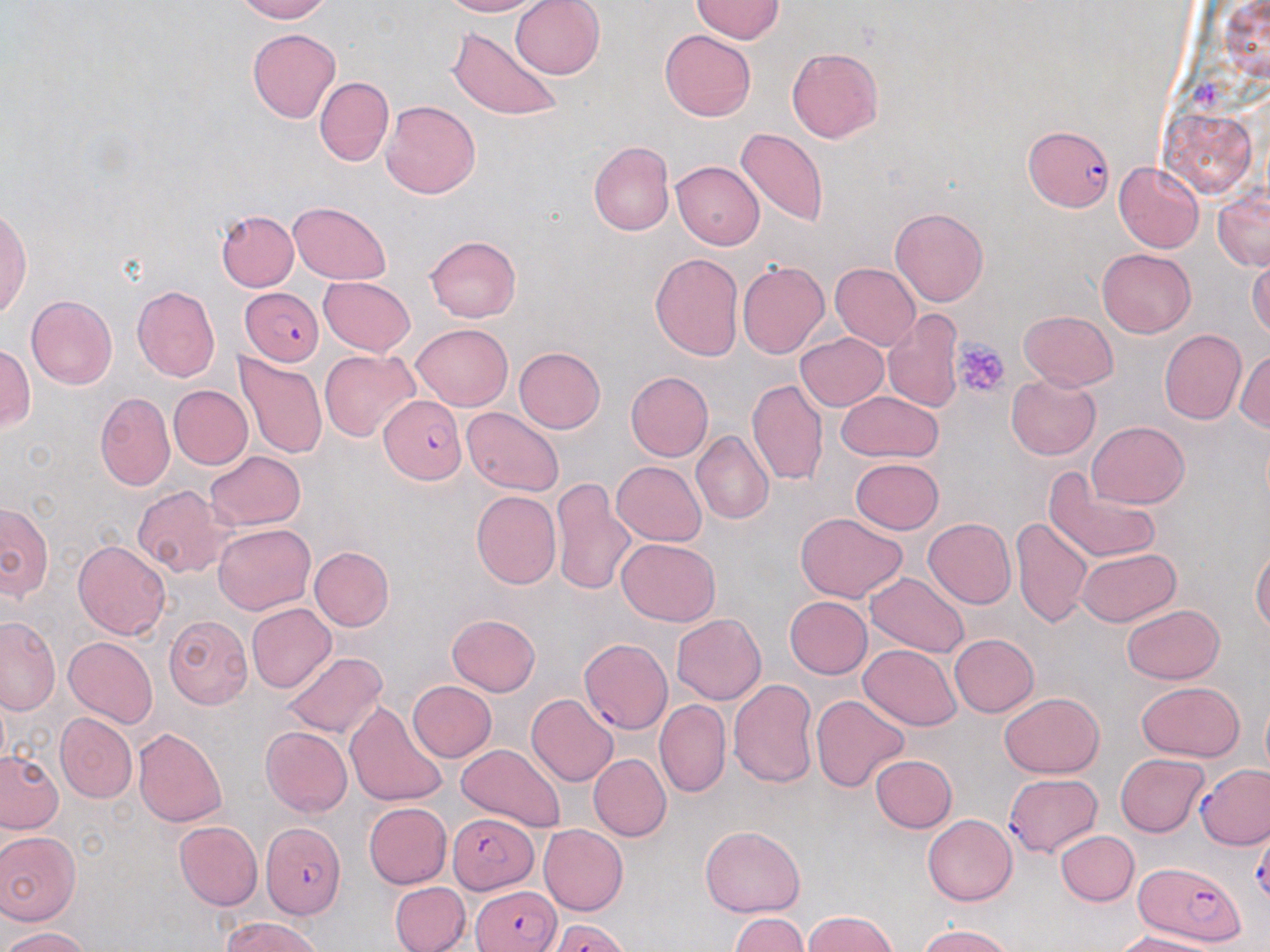 Approximate bounding boxes as (x1,y1)-(x2,y2) corner pairs in pixels. Uninfected red blood cell locations: (233,0)-(331,23), (439,0)-(540,17), (511,0)-(604,79), (692,0)-(784,43), (448,26)-(562,123), (248,28)-(341,123), (660,29)-(755,121), (786,47)-(884,144), (314,77)-(393,166), (381,100)-(481,199), (1159,108)-(1256,198), (736,127)-(829,229), (588,141)-(673,235), (672,160)-(763,251), (1114,162)-(1204,253), (1212,185)-(1270,271), (289,202)-(392,284), (0,206)-(32,322), (890,208)-(988,306), (215,209)-(298,291), (425,236)-(520,322), (1097,248)-(1196,338), (649,252)-(743,361), (1248,257)-(1270,338), (737,261)-(829,359), (831,263)-(921,349), (318,276)-(416,356), (132,285)-(220,382), (26,295)-(117,389), (1019,310)-(1117,391), (882,311)-(965,412), (411,323)-(512,410), (1159,331)-(1245,424), (795,332)-(889,411), (0,344)-(34,432), (513,347)-(605,433), (1234,348)-(1270,433), (320,349)-(419,440), (234,353)-(327,459), (625,371)-(713,462), (1006,374)-(1100,460), (747,379)-(828,488), (168,385)-(252,469), (836,390)-(942,462), (95,392)-(174,491), (463,406)-(564,496), (1087,422)-(1189,508), (691,431)-(773,525), (205,450)-(305,530), (852,457)-(944,534), (612,461)-(707,546), (1045,470)-(1161,565), (551,477)-(634,595), (132,486)-(235,578), (471,490)-(561,590), (0,502)-(54,600), (795,513)-(908,603), (1012,515)-(1093,628), (923,518)-(1016,609), (213,523)-(315,614), (615,538)-(722,626), (73,540)-(171,641), (310,546)-(394,630), (1251,547)-(1270,632), (1078,548)-(1181,626), (863,572)-(969,659), (784,596)-(872,679), (246,602)-(335,692), (1120,604)-(1225,684), (446,614)-(541,696), (164,615)-(254,709), (671,615)-(766,705), (0,616)-(60,713), (950,633)-(1039,716), (65,636)-(157,728), (858,644)-(962,731), (281,652)-(388,738), (728,680)-(819,788), (407,681)-(496,761), (1137,682)-(1245,761), (999,691)-(1104,778), (810,693)-(909,792), (527,694)-(618,787), (1260,697)-(1270,778), (344,699)-(448,807), (654,700)-(731,797), (55,712)-(137,804), (552,718)-(648,820), (133,726)-(227,827), (260,726)-(353,817), (457,743)-(567,833), (0,750)-(65,833), (1115,753)-(1208,835), (589,754)-(671,842), (870,755)-(957,832), (364,802)-(452,889), (923,813)-(1017,905), (173,821)-(263,911), (539,824)-(629,916), (699,824)-(805,917), (0,830)-(81,925), (1056,831)-(1139,906), (390,881)-(470,952), (803,910)-(900,952), (729,913)-(808,952), (221,915)-(327,952), (917,925)-(1015,952), (1,926)-(91,951), (1115,932)-(1220,952). Plasmodium falciparum-infected red blood cell locations: (1024,127)-(1113,211), (240,287)-(322,365), (381,393)-(465,484), (578,639)-(671,736), (1195,763)-(1270,849), (1004,774)-(1101,859), (448,811)-(539,895), (260,822)-(345,920), (1134,862)-(1247,945), (471,886)-(562,951), (551,919)-(629,952). Platelet locations: (953,338)-(1010,400). Slide-level diagnosis: Plasmodium falciparum. May-Grünwald-Giemsa stain. 1000x magnification. Thin blood smear. One field of a larger specimen. Light microscopy. Image is 1270×952 pixels.